Locate every white blood cell.
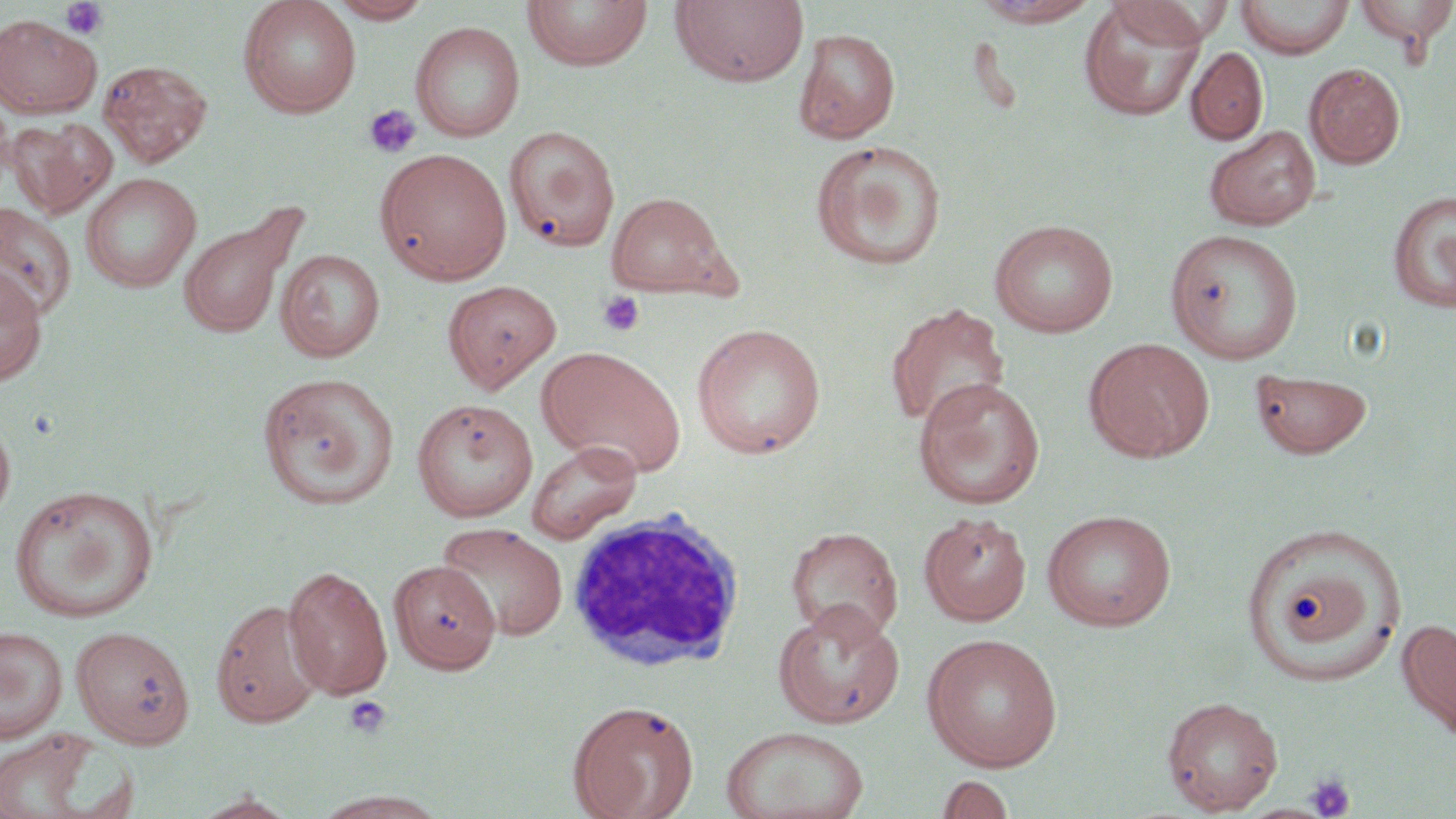

Approximate bounding boxes as (x1,y1)-(x2,y2) corner pairs in pixels.
White blood cells: (564,509)-(747,672).

Summary:
  - Platelet locations: (59,1)-(109,40), (363,104)-(422,158), (597,290)-(646,337), (345,696)-(391,738), (1305,773)-(1356,818)
  - Uninfected red blood cell locations: (238,0)-(361,119), (327,0)-(435,23), (522,0)-(653,72), (670,0)-(810,88), (1109,0)-(1226,48), (1235,0)-(1355,58), (1352,0)-(1456,56), (970,1)-(1102,27), (1079,2)-(1207,121), (0,13)-(102,119), (410,21)-(525,142), (794,27)-(901,144), (1186,47)-(1268,145), (98,59)-(212,168), (1304,62)-(1406,169), (7,117)-(117,218), (1204,125)-(1321,231), (504,128)-(617,252), (810,140)-(948,271), (376,148)-(512,285), (80,172)-(201,293), (1387,189)-(1456,315), (605,191)-(737,300), (177,200)-(307,341), (0,203)-(77,322), (989,218)-(1119,338), (1165,228)-(1304,364), (277,248)-(384,362), (0,266)-(47,387), (442,280)-(561,394), (885,302)-(1011,431), (691,322)-(827,460), (1083,337)-(1215,462), (536,345)-(686,477), (1250,368)-(1372,459), (258,371)-(399,508), (913,377)-(1045,509), (411,398)-(538,522), (0,414)-(16,528), (526,440)-(643,544), (9,484)-(160,622), (1042,509)-(1176,631), (919,512)-(1033,626), (1240,522)-(1407,685), (436,523)-(567,641), (786,526)-(904,643), (388,560)-(501,674), (282,565)-(393,699), (210,598)-(325,727), (774,603)-(905,728), (1396,617)-(1456,742), (71,625)-(195,749), (0,626)-(68,743), (921,633)-(1064,771), (1161,695)-(1284,815), (568,699)-(699,819), (720,725)-(871,819), (0,727)-(130,819), (937,773)-(1016,818), (308,791)-(453,819), (190,792)-(301,818)
  - Slide-level diagnosis: no evidence of blood parasites
  - Image size: 1456×819 pixels
  - Field of view: one of a larger specimen
  - Magnification: 1000x
  - Preparation: thin blood smear
  - Stain: May-Grünwald-Giemsa
  - Modality: light microscopy